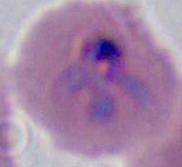

A Plasmodium parasite is seen. Micrograph. 400x or 1000x magnification.